Outline each P. falciparum parasite and classify it by life-cycle stage.
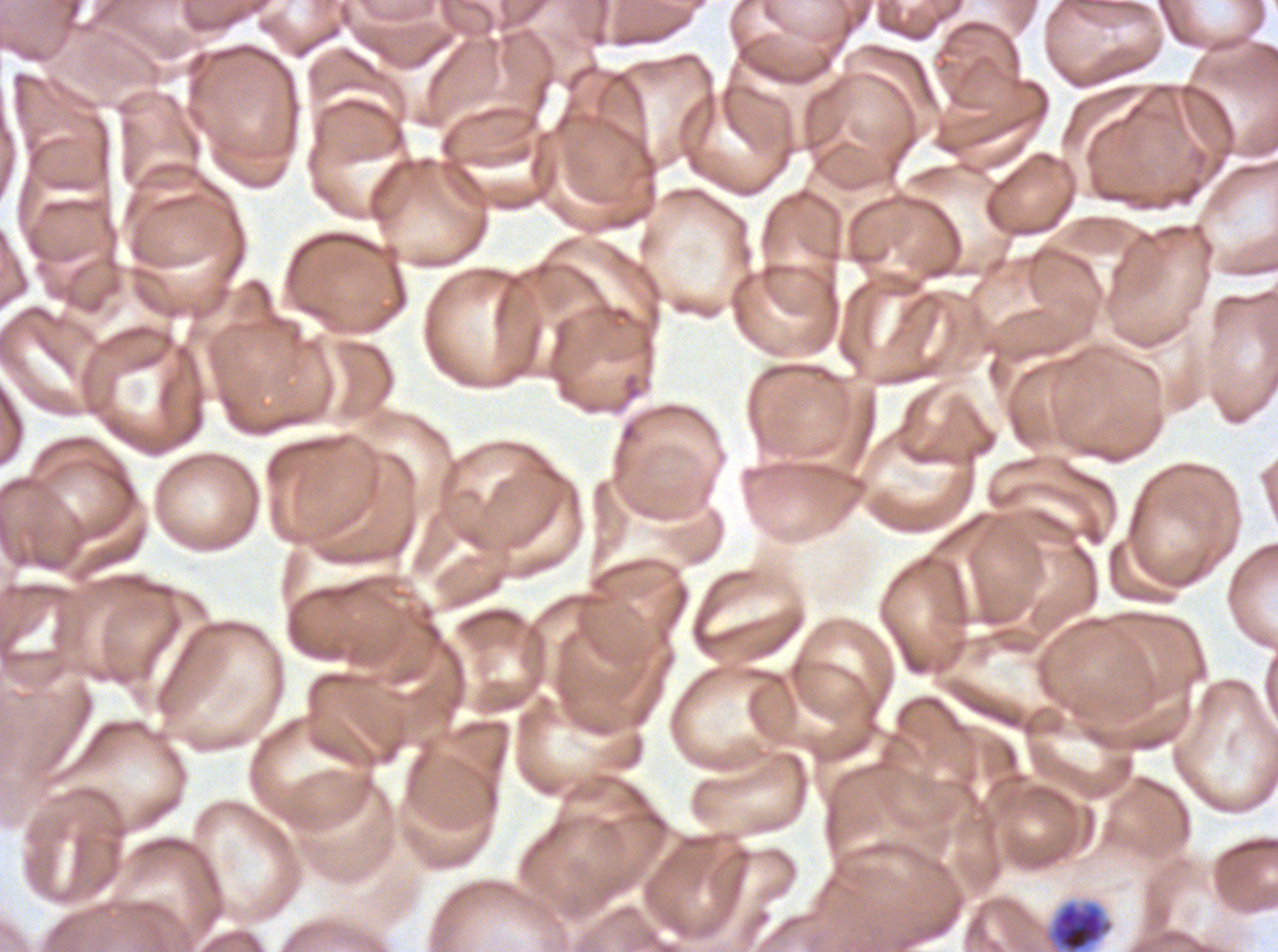
Approximate bounding boxes as (x1, y1, x2, y2) in pixels.
Segmenters: (1044, 899, 1114, 951).
No rings, late-ring/early-trophozoite forms, mid trophozoites, late trophozoites, early schizonts, late schizonts, or gametocytes observed.

Summary:
  - Image size: 1278×952 pixels
  - Stain: Giemsa
  - Specimen: P. falciparum from a patient in The Gambia, cultured ex vivo for 24 to 48 hours
  - Preparation: thin blood film
  - Field of view: one sub-image of a larger composite